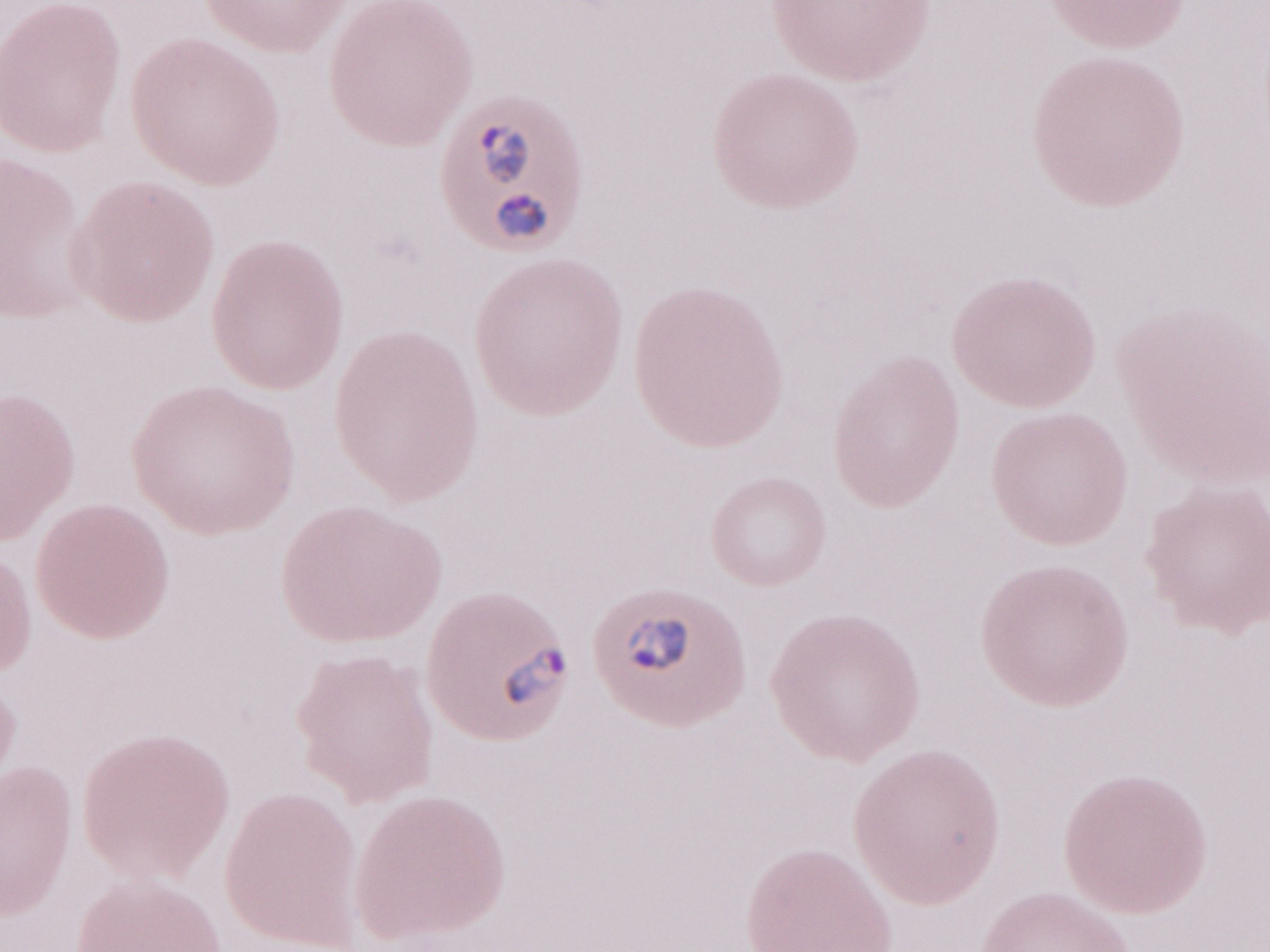

Olympus BX43 microscope, Olympus DP73 camera. Thin blood smear. May-Grünwald-Giemsa (MGG) stain. Image is 1270×952 pixels. One field of this slide. Patient-level malaria diagnosis: positive. Magnification: 1,000x.